Give the position of every Plasmodium parasite.
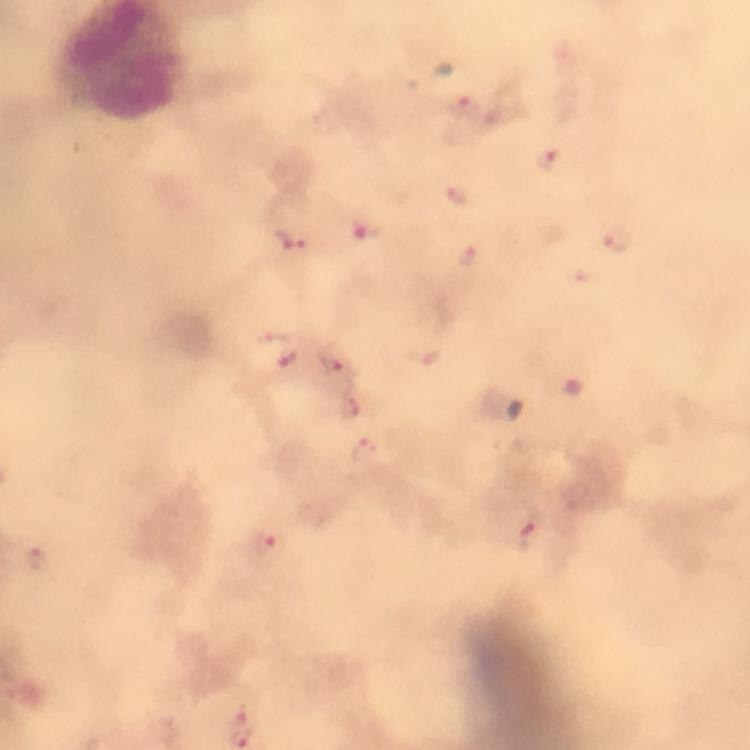

Approximate centers as (x, y) in pixels.
Plasmodium parasites: (463, 109), (546, 160), (458, 194), (367, 227), (289, 239), (617, 239), (467, 256), (271, 337), (289, 357), (332, 360), (578, 392), (349, 406), (364, 448), (526, 535), (271, 546), (35, 558), (245, 711).

Summary:
  - Cropped from: a single field of view
  - Immersion oil: used
  - Image size: 750×750 pixels
  - Stain: Giemsa
  - Capture: smartphone mounted on the microscope
  - Preparation: thick blood film
  - Magnification: 100x
  - Context: from a diagnostic examination for malaria